Identify the blood parasite species.
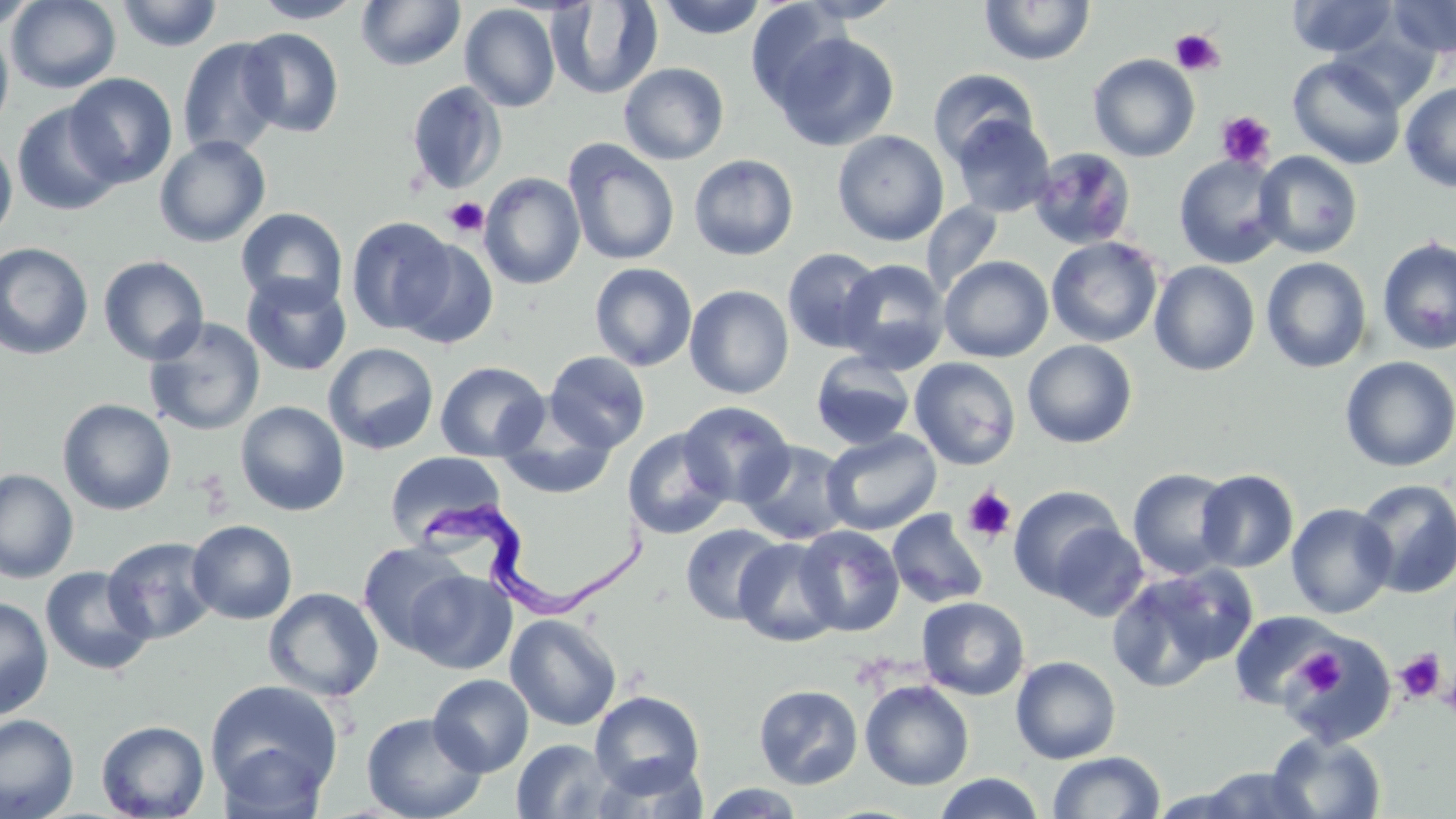
Trypanosoma brucei.

Summary:
  - Coordinate format: approximate bounding boxes as (x1,y1)-(x2,y2) corner pairs in pixels
  - Platelet locations: (1169,29)-(1225,76), (1216,111)-(1276,169), (443,197)-(489,238), (190,470)-(234,517), (962,486)-(1017,543), (1294,649)-(1347,697), (1394,650)-(1446,703), (1441,668)-(1456,724)
  - Uninfected red blood cell locations: (6,0)-(122,93), (252,0)-(365,23), (356,0)-(466,71), (548,0)-(662,99), (657,0)-(767,39), (796,0)-(905,23), (979,0)-(1096,66), (1288,0)-(1399,58), (1387,0)-(1456,58), (1,1)-(39,32), (115,1)-(224,52), (745,2)-(848,110), (459,3)-(561,112), (0,25)-(14,135), (238,28)-(345,137), (1332,28)-(1438,113), (771,31)-(900,151), (177,37)-(286,160), (1088,54)-(1200,162), (1287,55)-(1406,170), (618,62)-(729,165), (927,68)-(1041,166), (65,72)-(178,188), (405,80)-(508,195), (1400,81)-(1456,192), (13,102)-(125,215), (950,114)-(1055,218), (832,130)-(949,246), (0,135)-(17,243), (154,135)-(271,248), (563,139)-(680,266), (1029,147)-(1138,251), (1253,151)-(1363,258), (688,154)-(798,260), (1174,154)-(1286,269), (479,172)-(585,290), (922,202)-(1003,297), (235,207)-(348,311), (345,216)-(458,335), (1046,236)-(1163,347), (1377,236)-(1456,356), (394,238)-(499,349), (0,242)-(94,360), (782,248)-(884,352), (97,255)-(209,365), (939,255)-(1053,362), (1261,257)-(1372,373), (836,258)-(951,373), (1150,261)-(1260,376), (589,262)-(697,372), (241,273)-(352,377), (685,285)-(794,399), (143,317)-(266,436), (1022,339)-(1138,449), (323,342)-(439,455), (544,351)-(651,453), (810,351)-(916,450), (1339,356)-(1456,472), (909,357)-(1021,470), (435,361)-(549,462), (57,399)-(177,516), (235,400)-(350,517), (678,401)-(795,506), (496,409)-(620,500), (622,427)-(733,540), (821,429)-(942,535), (739,440)-(853,546), (385,451)-(508,548), (0,468)-(79,584), (1127,468)-(1237,580), (1195,469)-(1299,573), (1353,479)-(1456,599), (1008,484)-(1126,600), (1286,503)-(1396,618), (886,509)-(989,608), (186,520)-(298,625), (1046,522)-(1150,623), (680,523)-(787,626), (794,524)-(904,636), (102,536)-(219,644), (734,537)-(843,647), (358,541)-(472,652), (39,565)-(155,676), (1106,566)-(1253,693), (403,568)-(516,674), (263,587)-(384,701), (0,596)-(54,720), (917,597)-(1030,700), (1228,610)-(1346,711), (505,613)-(622,731), (1282,635)-(1397,747), (1011,656)-(1121,764), (428,673)-(534,777), (204,678)-(343,809), (859,680)-(974,790), (753,684)-(863,789), (590,690)-(706,796), (361,711)-(487,819), (0,714)-(79,819), (95,720)-(210,818), (1266,732)-(1387,818), (511,738)-(618,818), (216,741)-(330,819), (1047,751)-(1165,819), (1196,766)-(1318,818), (932,772)-(1045,819), (699,783)-(806,818), (1147,786)-(1253,818)
  - Trypanosoma brucei locations: (425,487)-(653,619)
  - Magnification: 1000x
  - Preparation: thin blood smear
  - Image size: 1456×819 pixels
  - Field of view: single
  - Stain: May-Grünwald-Giemsa
  - Modality: optical microscopy